Report the malaria status of this cell.
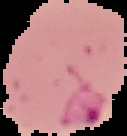

Parasitized.

Summary:
  - Image size: 127×136 pixels
  - Preparation: thin blood film
  - Image type: segmented cell region with the area outside set to black